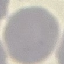

{
  "result": "no malaria parasites seen",
  "image_type": "automatically extracted cell patch, resized to 64 × 64 pixels",
  "preparation": "thin blood film",
  "stain": "Giemsa",
  "capture": "smartphone camera at the microscope eyepiece"
}